Locate every Plasmodium falciparum-infected red blood cell.
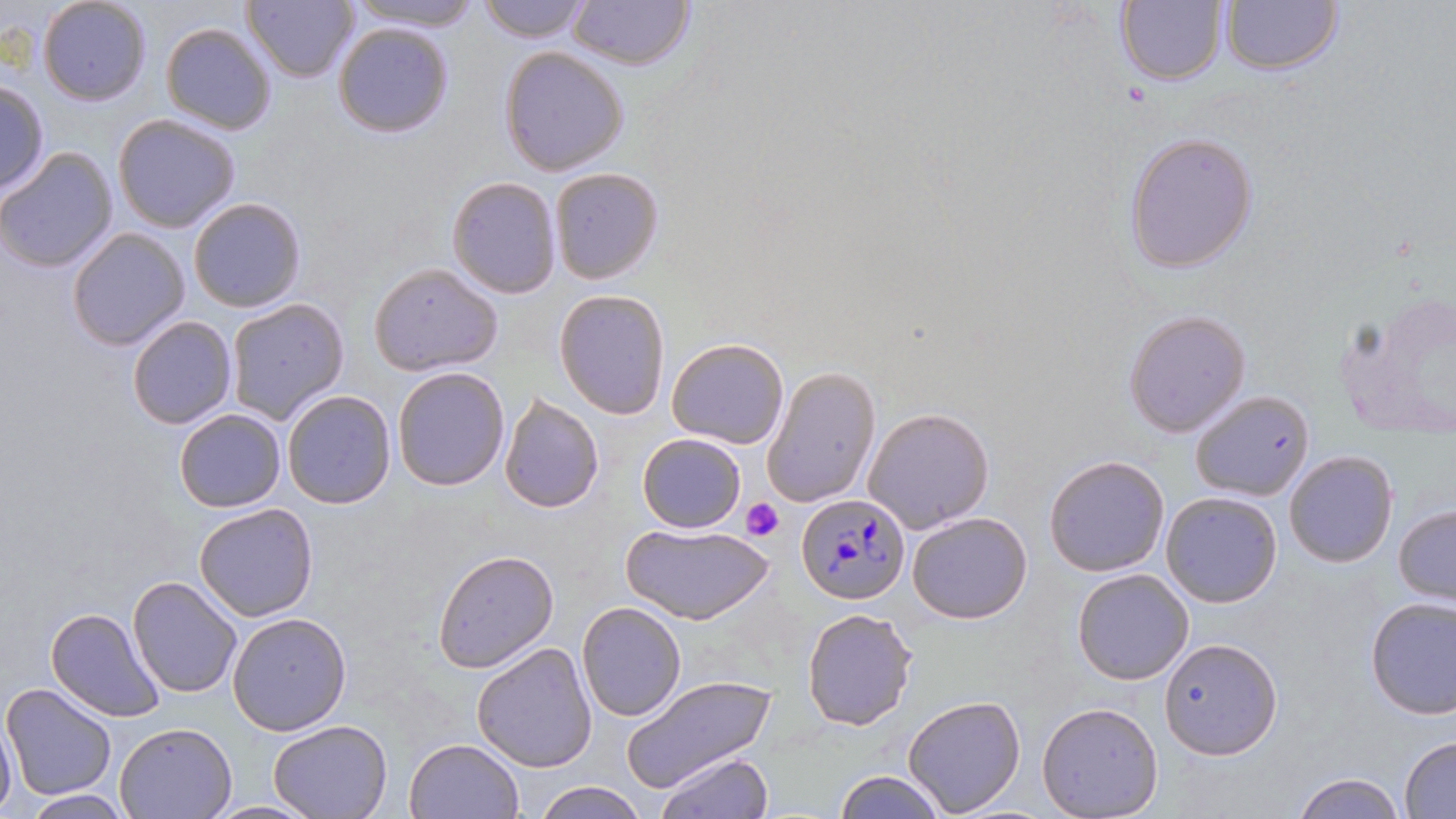

Approximate bounding boxes as named x1/y1/x2/y2 corners in pixels.
Plasmodium falciparum-infected red blood cells: (x1=793, y1=492, x2=911, y2=603).

Summary:
  - Platelet locations: (x1=740, y1=498, x2=783, y2=541)
  - Uninfected red blood cell locations: (x1=350, y1=0, x2=484, y2=31), (x1=568, y1=0, x2=696, y2=71), (x1=37, y1=1, x2=153, y2=106), (x1=243, y1=1, x2=358, y2=82), (x1=475, y1=1, x2=594, y2=44), (x1=1218, y1=1, x2=1344, y2=77), (x1=1116, y1=2, x2=1228, y2=85), (x1=333, y1=21, x2=453, y2=138), (x1=160, y1=22, x2=278, y2=134), (x1=500, y1=46, x2=630, y2=175), (x1=0, y1=81, x2=49, y2=196), (x1=112, y1=114, x2=242, y2=234), (x1=1123, y1=133, x2=1258, y2=272), (x1=0, y1=146, x2=119, y2=274), (x1=549, y1=168, x2=664, y2=283), (x1=447, y1=177, x2=562, y2=298), (x1=188, y1=198, x2=305, y2=313), (x1=67, y1=226, x2=191, y2=351), (x1=368, y1=262, x2=503, y2=377), (x1=1333, y1=287, x2=1456, y2=443), (x1=554, y1=288, x2=671, y2=418), (x1=224, y1=298, x2=350, y2=425), (x1=1124, y1=309, x2=1252, y2=437), (x1=126, y1=315, x2=237, y2=429), (x1=666, y1=338, x2=789, y2=449), (x1=390, y1=366, x2=509, y2=492), (x1=763, y1=366, x2=882, y2=507), (x1=1190, y1=388, x2=1315, y2=500), (x1=281, y1=389, x2=396, y2=510), (x1=498, y1=391, x2=606, y2=514), (x1=863, y1=406, x2=996, y2=533), (x1=173, y1=409, x2=287, y2=512), (x1=636, y1=434, x2=747, y2=532), (x1=1284, y1=450, x2=1398, y2=567), (x1=1043, y1=455, x2=1169, y2=575), (x1=1160, y1=491, x2=1285, y2=608), (x1=193, y1=503, x2=319, y2=621), (x1=1393, y1=505, x2=1456, y2=606), (x1=906, y1=511, x2=1032, y2=624), (x1=621, y1=522, x2=775, y2=625), (x1=431, y1=549, x2=560, y2=674), (x1=1071, y1=568, x2=1194, y2=684), (x1=129, y1=574, x2=242, y2=696), (x1=1365, y1=596, x2=1455, y2=719), (x1=576, y1=601, x2=686, y2=721), (x1=45, y1=607, x2=163, y2=722), (x1=802, y1=607, x2=917, y2=730), (x1=226, y1=611, x2=351, y2=736), (x1=1160, y1=636, x2=1280, y2=759), (x1=471, y1=641, x2=601, y2=773), (x1=622, y1=674, x2=774, y2=791), (x1=2, y1=682, x2=117, y2=799), (x1=903, y1=694, x2=1027, y2=817), (x1=1036, y1=701, x2=1165, y2=819), (x1=1, y1=708, x2=19, y2=819), (x1=266, y1=718, x2=393, y2=819), (x1=114, y1=720, x2=238, y2=817), (x1=1399, y1=736, x2=1456, y2=816), (x1=405, y1=738, x2=524, y2=819), (x1=652, y1=748, x2=774, y2=819), (x1=833, y1=770, x2=947, y2=818), (x1=1289, y1=773, x2=1409, y2=818), (x1=532, y1=779, x2=650, y2=818), (x1=20, y1=790, x2=129, y2=817), (x1=206, y1=799, x2=318, y2=817)
  - Slide-level diagnosis: Plasmodium falciparum
  - Preparation: thin blood film
  - Image size: 1456×819 pixels
  - Field of view: single
  - Magnification: 1000x
  - Modality: optical microscopy
  - Stain: May-Grünwald-Giemsa